Name the cell type shown.
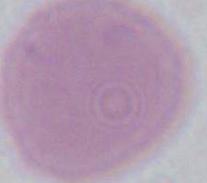

An erythrocyte.

1000x magnification. Photomicrograph.